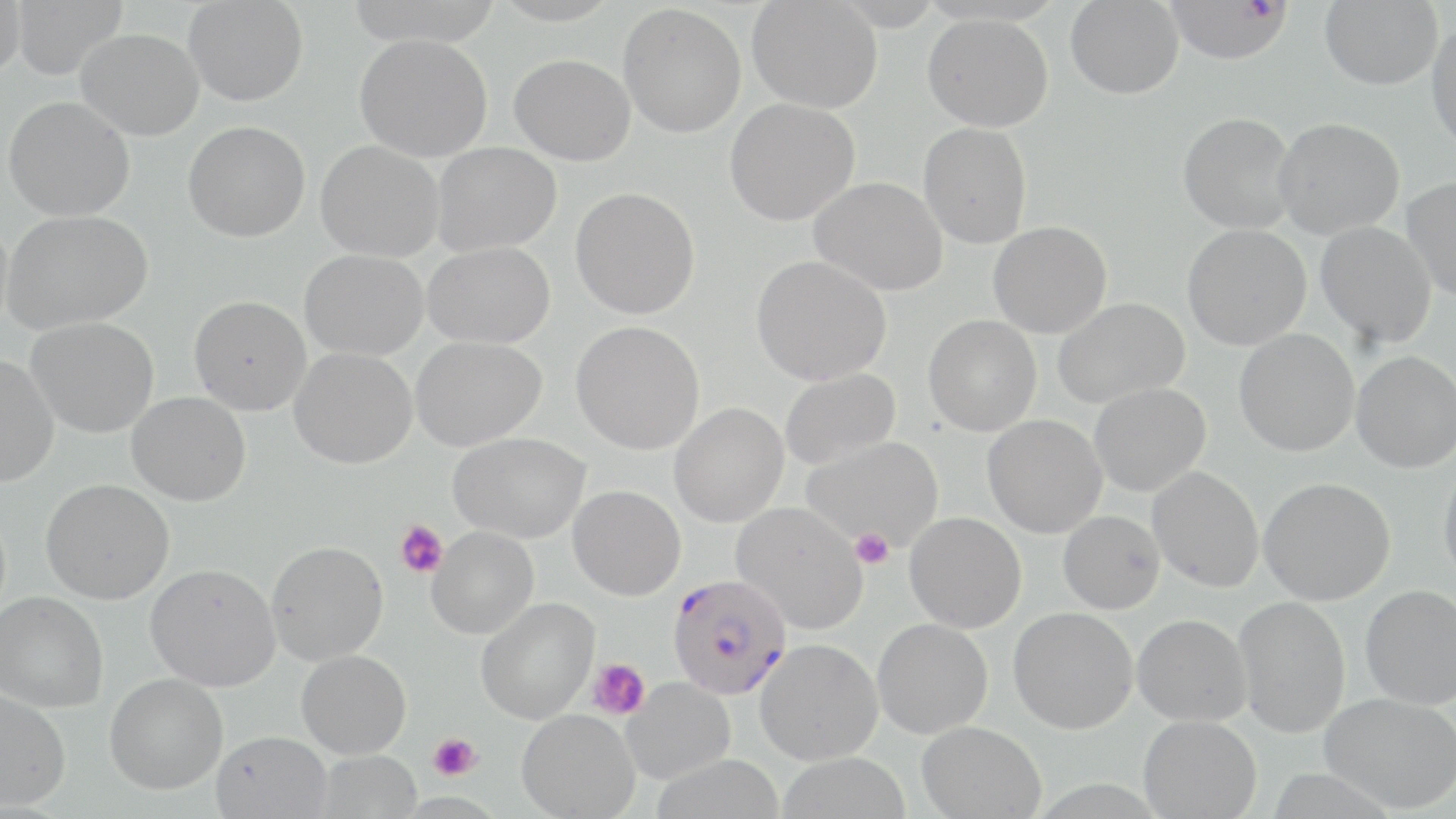
Approximate bounding boxes as (x1,y1)-(x2,y2) corner pairs in pixels. Uninfected red blood cell locations: (0,0)-(26,76), (11,0)-(128,80), (183,0)-(308,106), (747,0)-(882,113), (1065,0)-(1184,98), (1319,0)-(1443,90), (618,4)-(747,138), (922,13)-(1053,132), (1427,22)-(1456,155), (76,28)-(204,140), (355,33)-(493,161), (509,54)-(636,165), (3,96)-(135,222), (724,98)-(860,225), (1178,112)-(1297,234), (1273,117)-(1405,239), (183,121)-(310,242), (918,123)-(1032,248), (315,141)-(443,262), (432,142)-(561,255), (810,177)-(948,296), (1402,177)-(1456,301), (570,187)-(700,319), (2,209)-(153,333), (988,221)-(1112,338), (1316,221)-(1437,348), (1182,224)-(1312,350), (422,242)-(555,349), (299,249)-(428,361), (752,255)-(891,386), (188,295)-(310,415), (1053,297)-(1190,408), (923,315)-(1042,436), (25,317)-(159,438), (571,320)-(705,455), (1234,329)-(1360,457), (410,336)-(546,451), (289,347)-(417,469), (1351,351)-(1456,473), (0,354)-(59,487), (779,367)-(901,471), (1089,383)-(1211,496), (126,392)-(251,506), (669,402)-(789,527), (982,414)-(1108,538), (449,432)-(589,543), (803,437)-(941,551), (1438,462)-(1456,584), (1147,466)-(1264,592), (1259,477)-(1395,605), (40,478)-(174,605), (568,485)-(685,600), (731,501)-(868,634), (1058,510)-(1165,614), (905,512)-(1026,633), (426,526)-(538,639), (266,540)-(388,665), (145,564)-(280,692), (1360,585)-(1456,709), (0,591)-(109,713), (1234,596)-(1350,738), (476,597)-(599,724), (1008,607)-(1137,734), (1132,614)-(1251,725), (872,618)-(993,738), (755,639)-(883,765), (296,650)-(411,758), (104,673)-(228,795), (621,678)-(734,783), (0,691)-(71,810), (1319,691)-(1456,813), (517,709)-(640,819), (1138,715)-(1262,818), (917,720)-(1046,819), (211,730)-(332,819), (317,750)-(422,818), (776,752)-(912,818), (653,755)-(787,819). Platelet locations: (395,520)-(448,579), (850,528)-(894,568), (588,658)-(650,720), (428,733)-(481,780). Plasmodium falciparum-infected red blood cell locations: (1165,1)-(1294,64), (667,573)-(792,699). Slide-level diagnosis: Plasmodium falciparum. May-Grünwald-Giemsa-stained preparation. Captured at 1000x magnification. Thin blood film. Light microscopy. Single field of view. Image is 1456×819 pixels.